State which parasite is depicted.
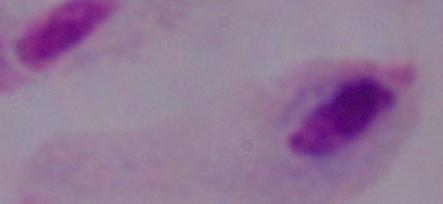

This is a trichomonad.

1000x magnification. Photomicrograph.